Describe the morphology of the red blood cells.
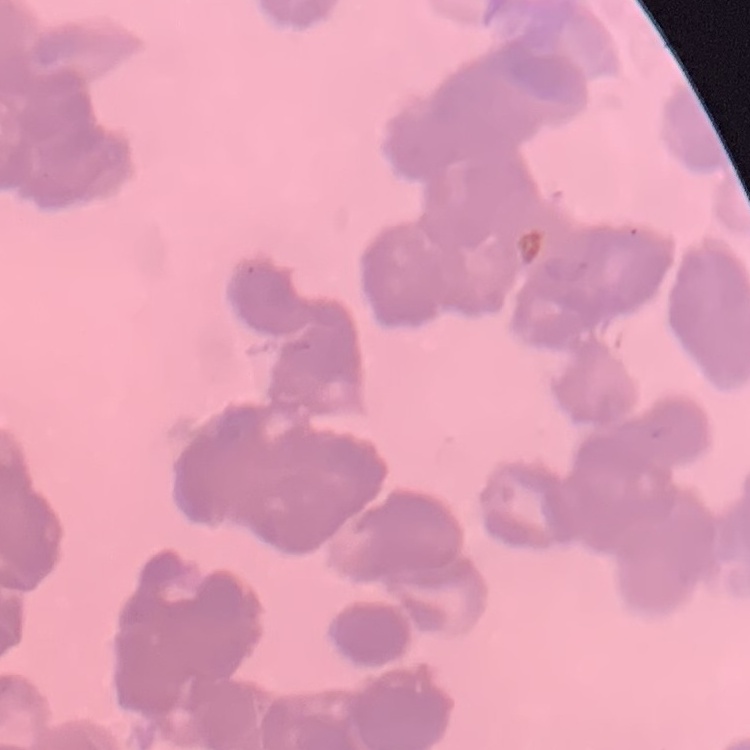
Rouleaux formation.

Square crop of a larger photomicrograph. Stained with either Field's or Giemsa. Thin blood film.